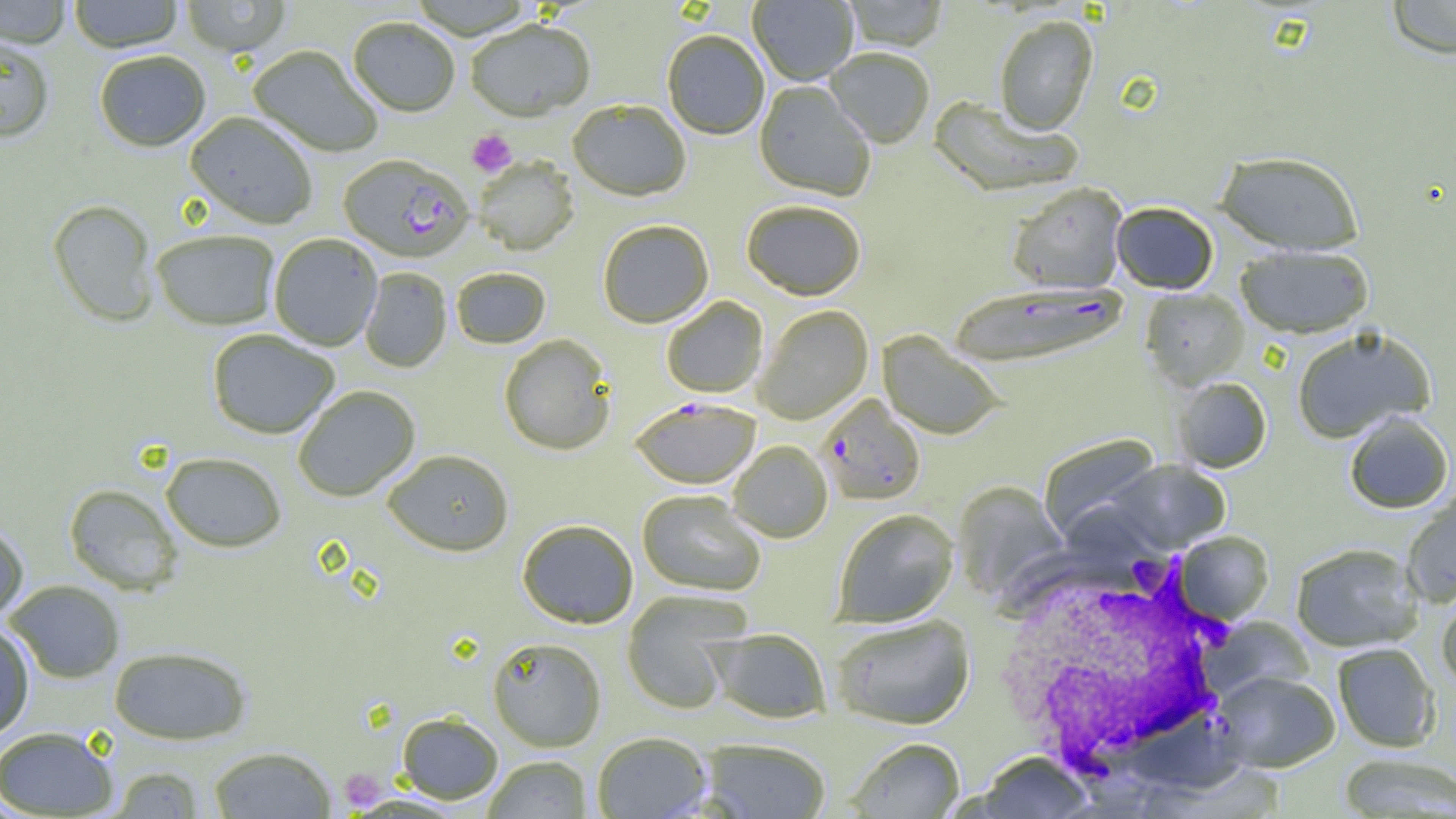

Summary:
  - Coordinate format: approximate bounding boxes as named x1/y1/x2/y2 corners in pixels
  - Platelet locations: (x1=467, y1=129, x2=516, y2=177), (x1=338, y1=768, x2=388, y2=810)
  - White blood cell locations: (x1=992, y1=551, x2=1238, y2=778)
  - Plasmodium falciparum-infected red blood cell locations: (x1=339, y1=155, x2=474, y2=264), (x1=948, y1=285, x2=1130, y2=370), (x1=817, y1=395, x2=925, y2=506), (x1=631, y1=399, x2=760, y2=490)
  - Uninfected red blood cell locations: (x1=0, y1=0, x2=71, y2=48), (x1=68, y1=0, x2=183, y2=53), (x1=180, y1=0, x2=291, y2=58), (x1=748, y1=0, x2=858, y2=86), (x1=842, y1=0, x2=948, y2=53), (x1=1384, y1=0, x2=1456, y2=59), (x1=994, y1=15, x2=1099, y2=136), (x1=348, y1=18, x2=460, y2=119), (x1=466, y1=22, x2=595, y2=124), (x1=662, y1=32, x2=768, y2=141), (x1=0, y1=36, x2=55, y2=143), (x1=247, y1=46, x2=382, y2=158), (x1=824, y1=49, x2=934, y2=149), (x1=93, y1=50, x2=211, y2=152), (x1=754, y1=82, x2=875, y2=202), (x1=929, y1=98, x2=1082, y2=198), (x1=568, y1=102, x2=691, y2=203), (x1=184, y1=113, x2=318, y2=230), (x1=1216, y1=151, x2=1364, y2=255), (x1=473, y1=158, x2=579, y2=257), (x1=1006, y1=183, x2=1128, y2=294), (x1=46, y1=199, x2=160, y2=327), (x1=741, y1=202, x2=866, y2=301), (x1=1111, y1=202, x2=1219, y2=294), (x1=598, y1=221, x2=713, y2=329), (x1=151, y1=230, x2=280, y2=330), (x1=269, y1=234, x2=382, y2=351), (x1=1235, y1=245, x2=1375, y2=339), (x1=451, y1=267, x2=551, y2=349), (x1=360, y1=268, x2=451, y2=373), (x1=1141, y1=289, x2=1250, y2=390), (x1=661, y1=297, x2=768, y2=398), (x1=755, y1=306, x2=873, y2=424), (x1=1292, y1=326, x2=1436, y2=443), (x1=207, y1=329, x2=338, y2=439), (x1=877, y1=331, x2=1006, y2=440), (x1=498, y1=335, x2=615, y2=455), (x1=1174, y1=377, x2=1272, y2=473), (x1=293, y1=386, x2=421, y2=502), (x1=1343, y1=411, x2=1454, y2=514), (x1=1039, y1=434, x2=1163, y2=542), (x1=728, y1=441, x2=833, y2=543), (x1=382, y1=450, x2=514, y2=558), (x1=160, y1=452, x2=287, y2=552), (x1=1105, y1=460, x2=1231, y2=554), (x1=952, y1=481, x2=1069, y2=602), (x1=64, y1=484, x2=183, y2=595), (x1=637, y1=490, x2=765, y2=596), (x1=1401, y1=491, x2=1456, y2=607), (x1=832, y1=508, x2=959, y2=627), (x1=517, y1=520, x2=639, y2=630), (x1=0, y1=522, x2=29, y2=621), (x1=1175, y1=531, x2=1274, y2=624), (x1=1290, y1=543, x2=1424, y2=653), (x1=5, y1=579, x2=125, y2=683), (x1=621, y1=591, x2=749, y2=714), (x1=1436, y1=591, x2=1456, y2=694), (x1=831, y1=614, x2=976, y2=730), (x1=1205, y1=616, x2=1314, y2=700), (x1=0, y1=623, x2=35, y2=740), (x1=706, y1=628, x2=832, y2=724), (x1=488, y1=637, x2=606, y2=751), (x1=1332, y1=642, x2=1440, y2=752), (x1=109, y1=645, x2=252, y2=745), (x1=1215, y1=671, x2=1340, y2=772), (x1=396, y1=712, x2=503, y2=804), (x1=0, y1=726, x2=119, y2=817), (x1=592, y1=731, x2=713, y2=819), (x1=847, y1=737, x2=965, y2=818), (x1=701, y1=738, x2=831, y2=818), (x1=207, y1=746, x2=337, y2=818), (x1=975, y1=752, x2=1093, y2=818), (x1=1338, y1=753, x2=1455, y2=818), (x1=483, y1=755, x2=593, y2=818), (x1=106, y1=766, x2=205, y2=818)
  - Slide-level diagnosis: Plasmodium falciparum
  - Modality: optical microscopy
  - Magnification: 1000x
  - Preparation: thin blood film
  - Field of view: one of a larger specimen
  - Image size: 1456×819 pixels